Give the extent of all Plasmodium vivax-infected red blood cells.
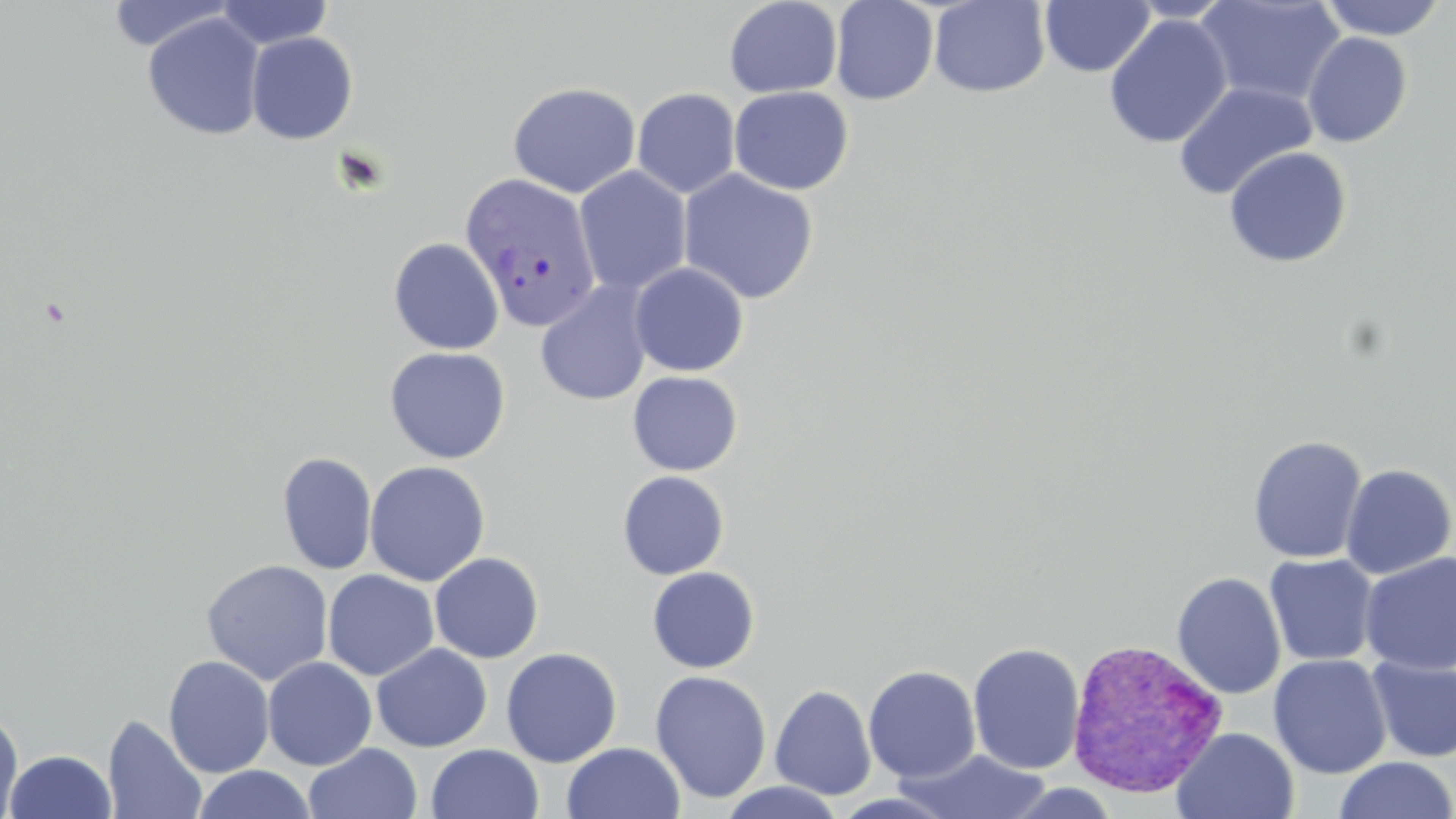
Approximate bounding boxes as named x1/y1/x2/y2 corners in pixels.
Plasmodium vivax-infected red blood cells: (x1=459, y1=171, x2=601, y2=332), (x1=1070, y1=642, x2=1231, y2=802).

Uninfected red blood cell locations: (x1=106, y1=0, x2=237, y2=54), (x1=215, y1=0, x2=333, y2=49), (x1=724, y1=0, x2=842, y2=98), (x1=830, y1=0, x2=939, y2=105), (x1=928, y1=0, x2=1051, y2=98), (x1=1124, y1=0, x2=1238, y2=23), (x1=1195, y1=0, x2=1346, y2=107), (x1=1317, y1=0, x2=1447, y2=40), (x1=1039, y1=1, x2=1155, y2=77), (x1=142, y1=12, x2=266, y2=141), (x1=1103, y1=14, x2=1232, y2=149), (x1=246, y1=31, x2=358, y2=144), (x1=1302, y1=32, x2=1413, y2=148), (x1=508, y1=81, x2=641, y2=198), (x1=1172, y1=81, x2=1317, y2=201), (x1=728, y1=85, x2=854, y2=195), (x1=632, y1=88, x2=741, y2=199), (x1=1223, y1=146, x2=1353, y2=268), (x1=574, y1=166, x2=692, y2=296), (x1=678, y1=169, x2=819, y2=304), (x1=388, y1=238, x2=505, y2=355), (x1=630, y1=262, x2=749, y2=377), (x1=536, y1=281, x2=654, y2=406), (x1=384, y1=346, x2=511, y2=465), (x1=627, y1=371, x2=743, y2=476), (x1=1247, y1=434, x2=1368, y2=563), (x1=276, y1=451, x2=377, y2=575), (x1=365, y1=461, x2=490, y2=586), (x1=1340, y1=463, x2=1455, y2=579), (x1=617, y1=470, x2=729, y2=580), (x1=429, y1=552, x2=544, y2=663), (x1=1359, y1=552, x2=1456, y2=675), (x1=1264, y1=553, x2=1379, y2=667), (x1=201, y1=559, x2=334, y2=686), (x1=646, y1=566, x2=760, y2=673), (x1=322, y1=569, x2=439, y2=681), (x1=1171, y1=572, x2=1287, y2=700), (x1=967, y1=642, x2=1086, y2=775), (x1=371, y1=643, x2=493, y2=752), (x1=501, y1=647, x2=622, y2=767), (x1=1268, y1=654, x2=1392, y2=779), (x1=163, y1=655, x2=275, y2=778), (x1=1366, y1=656, x2=1456, y2=763), (x1=262, y1=657, x2=377, y2=771), (x1=863, y1=664, x2=981, y2=782), (x1=649, y1=670, x2=772, y2=803), (x1=769, y1=684, x2=876, y2=800), (x1=0, y1=710, x2=24, y2=818), (x1=103, y1=714, x2=207, y2=818), (x1=1171, y1=727, x2=1300, y2=818), (x1=561, y1=742, x2=685, y2=819), (x1=304, y1=743, x2=423, y2=819), (x1=427, y1=744, x2=544, y2=819), (x1=4, y1=749, x2=116, y2=818), (x1=895, y1=749, x2=1053, y2=819), (x1=1333, y1=756, x2=1456, y2=819), (x1=192, y1=765, x2=316, y2=819), (x1=717, y1=781, x2=847, y2=818), (x1=1000, y1=782, x2=1123, y2=818), (x1=831, y1=792, x2=955, y2=819). Slide-level diagnosis: Plasmodium vivax. Image is 1456×819 pixels. Optical microscopy. One field of a larger specimen. Captured at 1000x magnification. Thin blood smear. May-Grünwald-Giemsa-stained preparation.